Give the extent of all Plasmodium malariae-infected red blood cells.
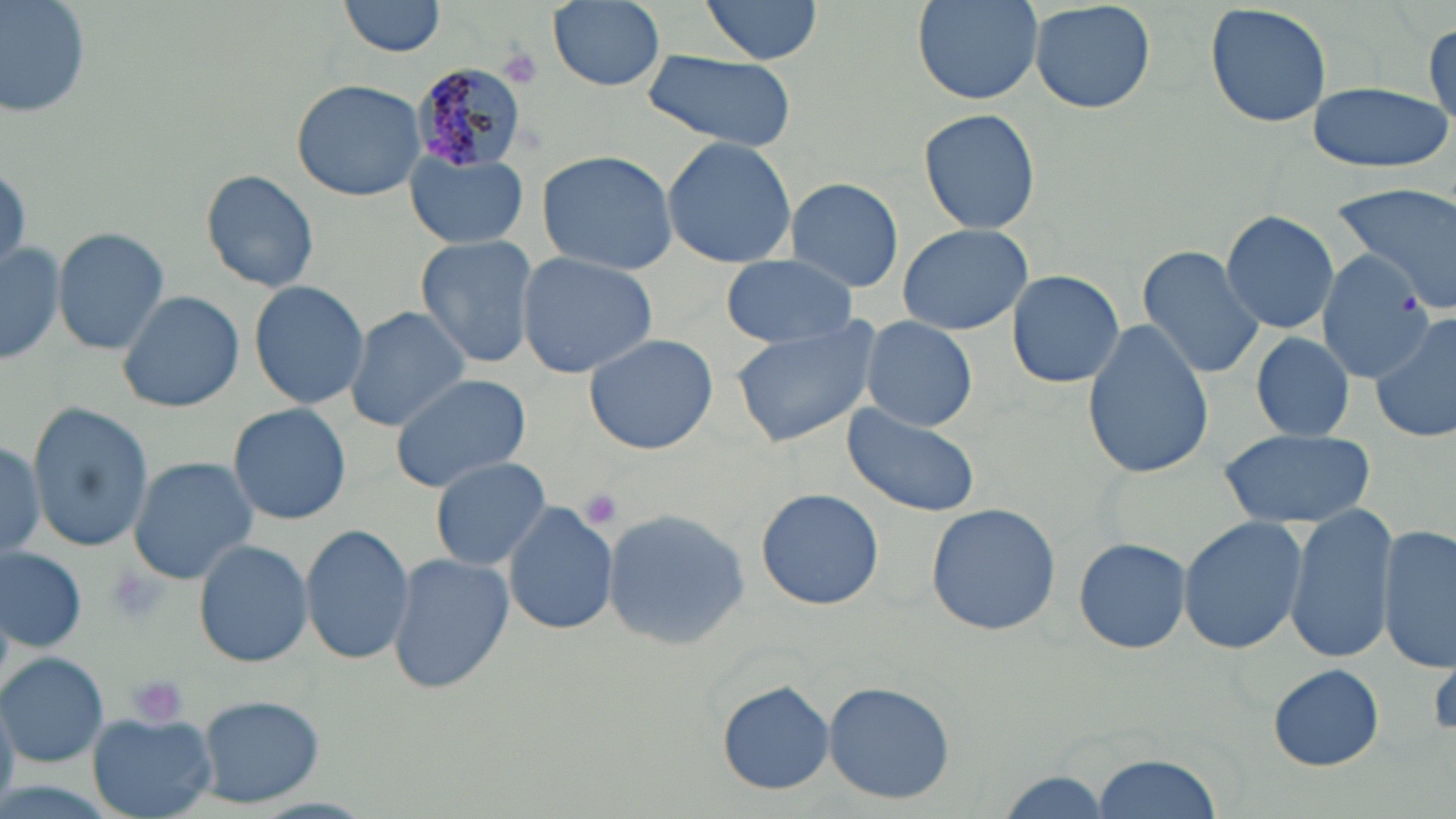

Approximate bounding boxes as (x1,y1)-(x2,y2) corner pairs in pixels.
Plasmodium malariae-infected red blood cells: (407,64)-(529,173).

Summary:
  - Uninfected red blood cell locations: (1,0)-(89,122), (340,0)-(448,58), (700,0)-(822,65), (911,0)-(1046,105), (1028,0)-(1156,115), (548,1)-(665,89), (1206,2)-(1332,130), (1425,22)-(1456,135), (643,50)-(795,153), (292,79)-(425,201), (1305,80)-(1452,173), (918,106)-(1040,235), (661,135)-(798,267), (406,150)-(530,250), (536,150)-(677,275), (199,168)-(320,292), (784,175)-(905,292), (1332,184)-(1456,315), (1220,209)-(1341,335), (897,222)-(1034,336), (52,226)-(171,356), (413,234)-(539,368), (1,239)-(64,368), (1137,243)-(1264,380), (1319,252)-(1437,386), (516,253)-(658,378), (721,257)-(858,348), (1006,269)-(1126,389), (247,280)-(370,411), (117,288)-(244,412), (343,306)-(472,430), (1371,312)-(1456,444), (730,316)-(883,448), (859,316)-(978,430), (1082,319)-(1213,480), (583,332)-(719,455), (1250,332)-(1355,441), (389,373)-(537,493), (26,402)-(154,552), (227,402)-(352,525), (843,405)-(982,519), (1217,428)-(1375,530), (0,435)-(46,562), (127,457)-(258,581), (431,458)-(552,570), (754,488)-(884,611), (504,501)-(617,635), (925,502)-(1063,635), (1285,504)-(1396,663), (601,510)-(752,651), (1177,518)-(1307,655), (300,523)-(414,664), (1379,523)-(1455,674), (1071,535)-(1192,655), (193,538)-(314,667), (1,545)-(87,654), (385,553)-(514,694), (0,653)-(108,765), (1268,663)-(1385,771), (822,680)-(956,805), (716,681)-(834,794), (193,693)-(326,809), (86,711)-(217,817), (1094,751)-(1223,819), (992,772)-(1113,816)
  - Platelet locations: (497,46)-(543,90), (577,486)-(625,529), (103,563)-(169,626), (128,676)-(188,729)
  - Slide-level diagnosis: Plasmodium malariae
  - Stain: May-Grünwald-Giemsa
  - Preparation: thin blood film
  - Image size: 1456×819 pixels
  - Magnification: 1000x
  - Modality: light microscopy
  - Field of view: single